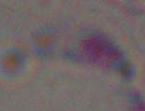 Micrograph. Captured at 1000x magnification. Toxoplasma gondii is shown.